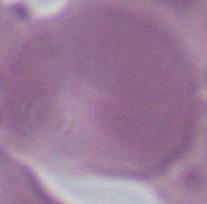
magnification = 1000x
identification = red blood cell
modality = micrograph